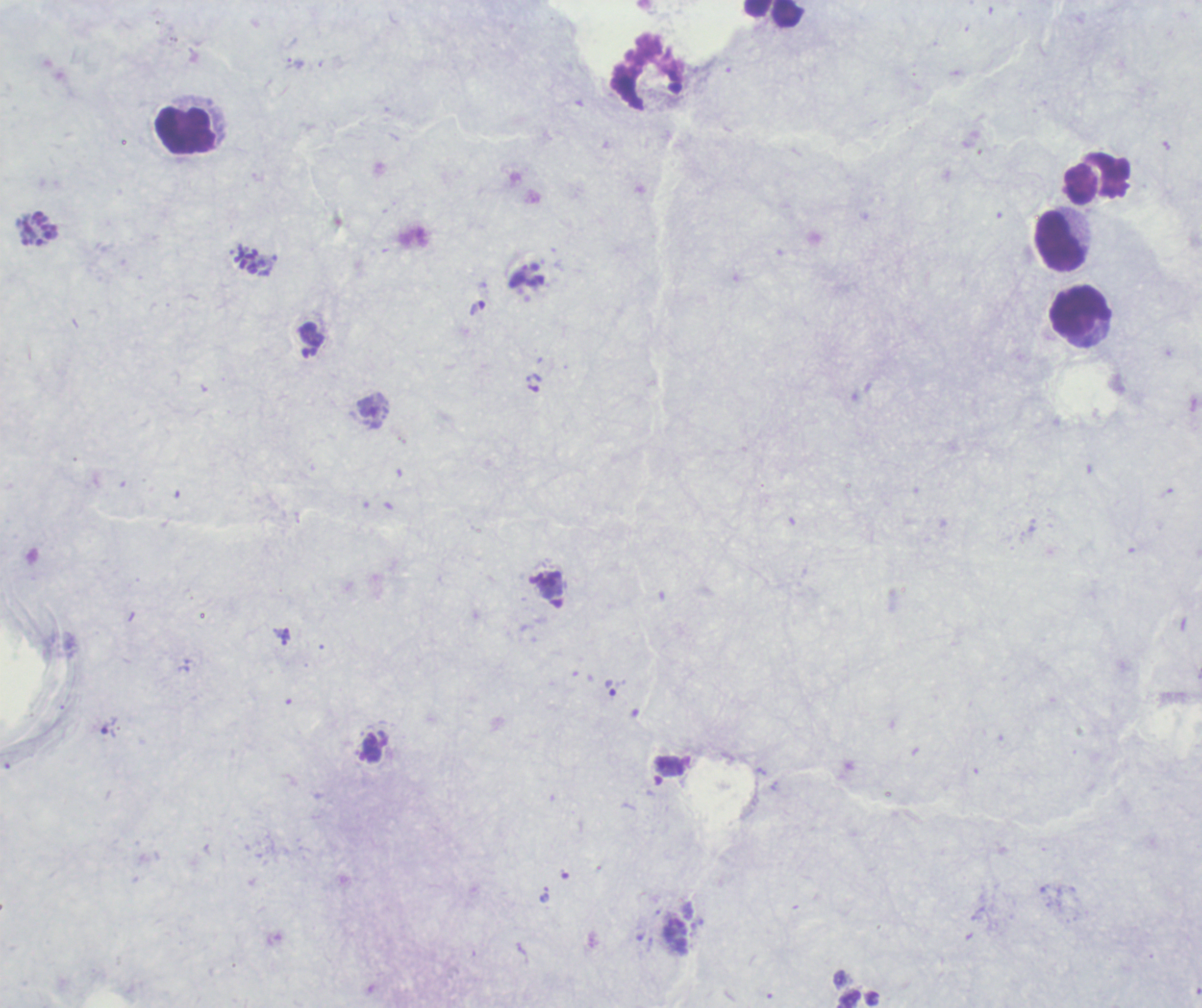
{
  "life_cycle_stages_observed": "trophozoite, schizont",
  "trophozoite_locations": "approximate centers as {x, y} in pixels: {285, 633}, {610, 688}, {108, 728}",
  "stain": "Romanowsky",
  "preparation": "thick blood smear",
  "context": "previously used in an actual diagnosis",
  "result": "Plasmodium parasites identified",
  "field_of_view": "one from this slide",
  "background_quality": "poor",
  "magnification": "100x",
  "image_size": "1202×1008 pixels",
  "schizont_locations": "approximate centers as {x, y} in pixels: {38, 228}, {248, 261}, {548, 579}",
  "leukocyte_locations": "approximate centers as {x, y} in pixels: {774, 14}, {186, 130}, {1098, 180}, {1060, 242}, {1081, 311}"
}